Locate every Babesia divergens-infected red blood cell.
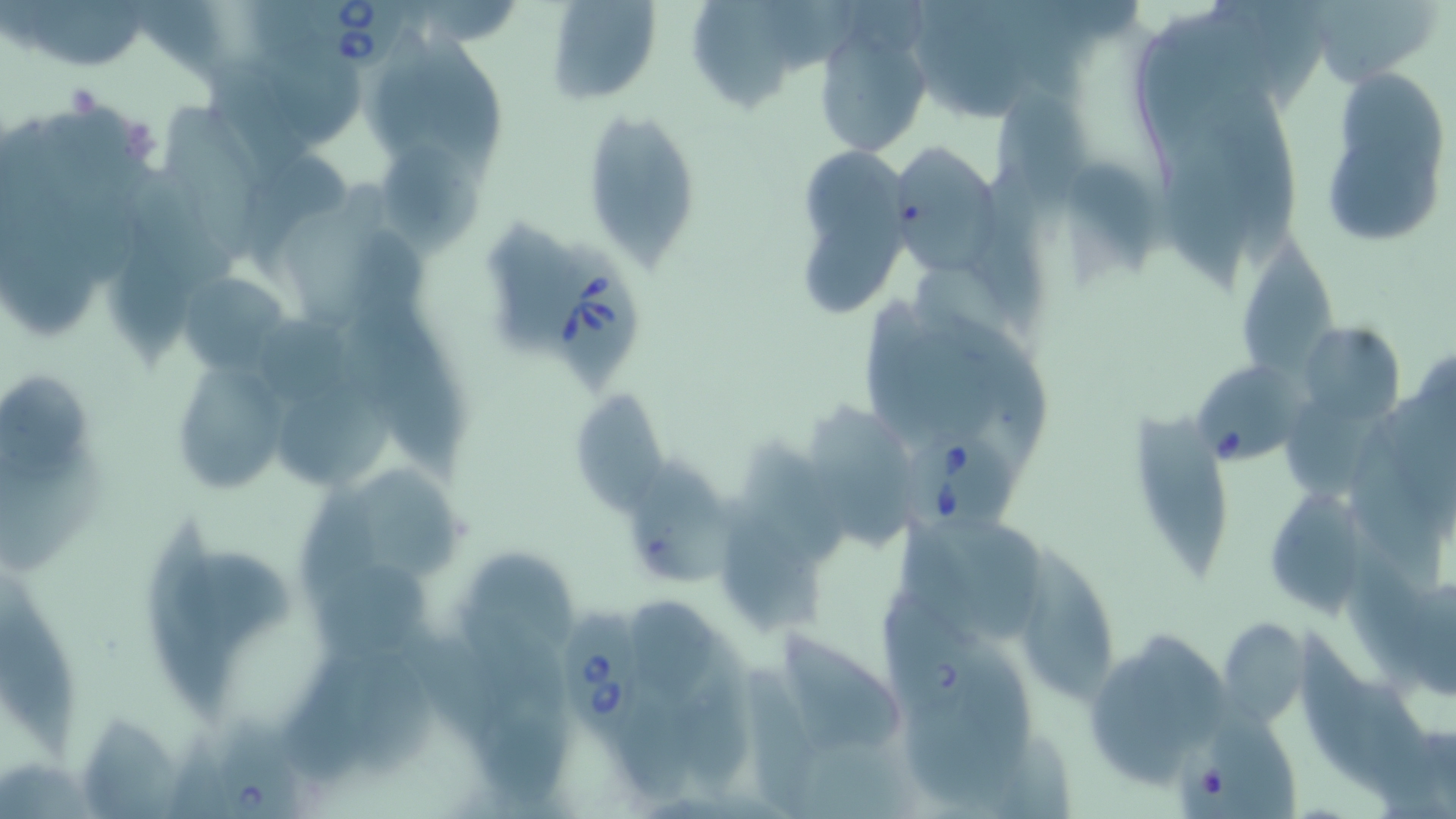
Approximate bounding boxes as [x1, y1, x2, y2] in pixels.
Babesia divergens-infected red blood cells: [302, 0, 414, 75], [538, 235, 643, 397], [1197, 361, 1298, 474], [889, 419, 1017, 546], [552, 604, 655, 763], [213, 724, 305, 819].

Uninfected red blood cell locations: [545, 0, 662, 106], [692, 0, 795, 113], [1304, 1, 1442, 87], [813, 25, 930, 157], [270, 37, 367, 153], [1319, 66, 1452, 249], [992, 81, 1096, 247], [580, 108, 703, 270], [882, 138, 1006, 271], [381, 146, 486, 261], [807, 206, 906, 315], [105, 229, 200, 365], [1242, 240, 1339, 381], [183, 277, 290, 376], [366, 314, 463, 480], [1306, 321, 1403, 421], [174, 367, 285, 491], [570, 388, 672, 516], [276, 390, 396, 486], [810, 408, 922, 549], [1129, 413, 1227, 584], [630, 459, 730, 585], [363, 467, 462, 584], [1270, 492, 1369, 620], [719, 500, 826, 632], [922, 521, 1054, 634], [148, 524, 234, 720], [1016, 547, 1112, 705], [473, 553, 567, 646], [0, 570, 76, 761], [313, 571, 429, 658], [624, 596, 719, 701], [1217, 616, 1308, 727], [776, 633, 896, 740], [282, 658, 387, 780], [746, 673, 821, 819]. Slide-level diagnosis: Babesia divergens. 1000x magnification. Optical microscopy. May-Grünwald-Giemsa stain. Thin blood film. One field of a larger specimen. Image is 1456×819 pixels.